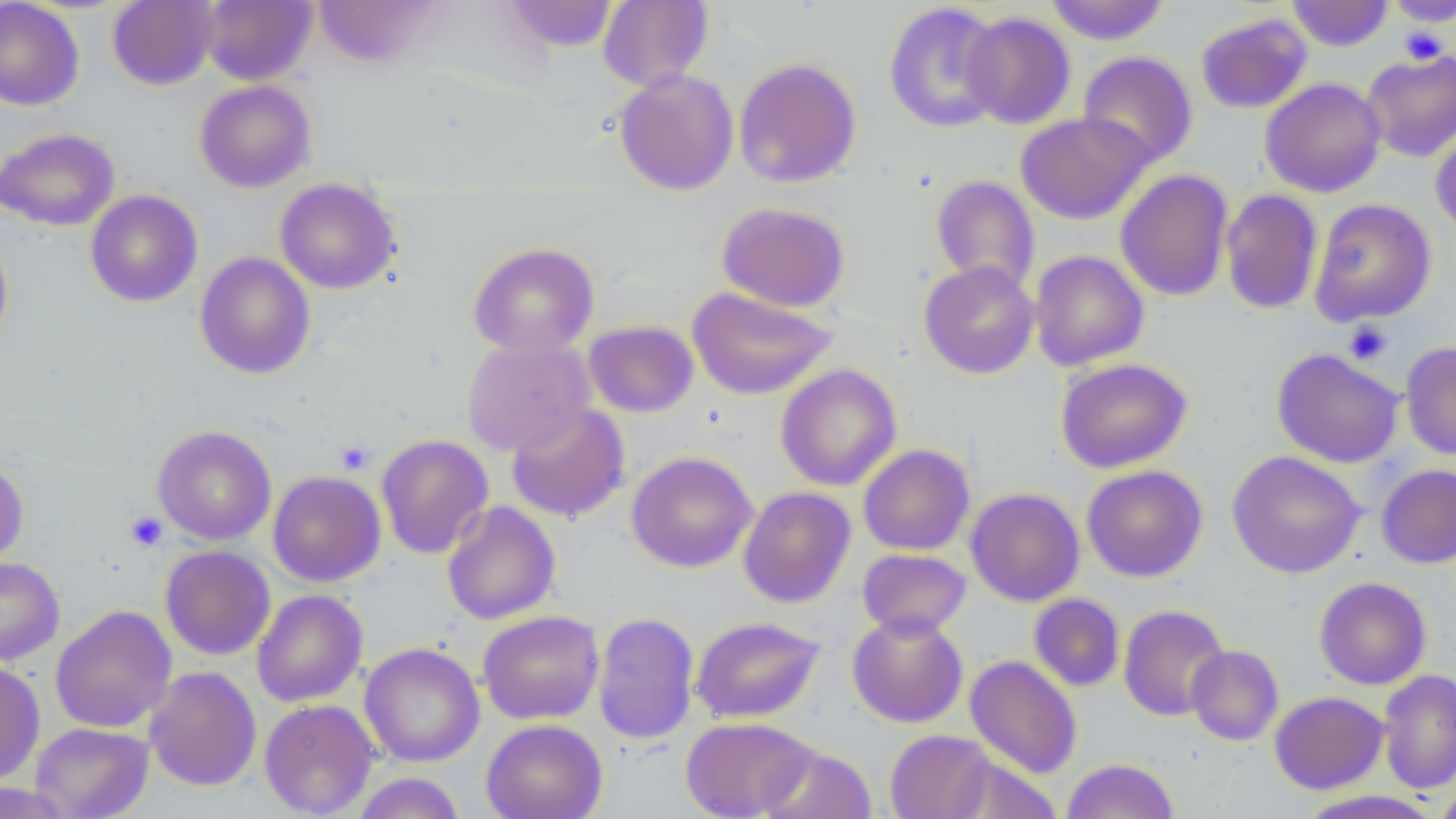

Approximate bounding boxes as (x1,y1)-(x2,y2) corner pairs in pixels. Uninfected red blood cell locations: (107,0)-(219,90), (200,0)-(316,86), (502,0)-(618,53), (598,0)-(713,92), (1046,0)-(1169,45), (1286,0)-(1394,52), (1384,0)-(1456,28), (0,1)-(85,111), (883,2)-(1005,133), (961,12)-(1076,129), (1195,12)-(1312,114), (1360,49)-(1456,162), (1077,51)-(1198,169), (734,58)-(861,188), (614,68)-(739,196), (1260,78)-(1387,197), (194,80)-(316,193), (1015,112)-(1153,224), (1430,120)-(1456,238), (0,127)-(120,231), (1115,169)-(1233,301), (931,175)-(1040,293), (274,178)-(402,294), (1220,189)-(1323,315), (84,190)-(202,308), (1309,198)-(1436,326), (717,201)-(850,312), (0,226)-(14,351), (467,241)-(599,357), (1029,250)-(1149,371), (195,252)-(316,379), (919,260)-(1039,379), (687,287)-(837,400), (584,320)-(699,417), (461,338)-(595,456), (1400,341)-(1456,460), (1272,348)-(1403,468), (1055,358)-(1192,473), (775,363)-(902,491), (505,402)-(631,523), (152,425)-(276,545), (376,433)-(494,559), (857,444)-(974,556), (1227,450)-(1364,578), (626,451)-(758,572), (0,458)-(29,565), (1376,463)-(1456,569), (1081,465)-(1207,582), (267,470)-(386,586), (738,486)-(856,608), (965,487)-(1085,607), (441,501)-(561,625), (160,545)-(275,660), (857,548)-(972,638), (0,556)-(65,666), (1314,576)-(1432,690), (252,589)-(368,707), (1028,593)-(1125,692), (1118,604)-(1231,721), (50,605)-(177,733), (478,610)-(605,724), (847,610)-(968,728), (593,612)-(700,746), (690,616)-(825,723), (360,642)-(484,767), (1186,645)-(1284,745), (965,655)-(1082,779), (0,659)-(45,785), (144,667)-(262,792), (1378,669)-(1456,794), (1269,691)-(1388,794), (259,699)-(379,817), (680,717)-(814,819), (481,719)-(607,819), (30,723)-(154,819), (884,729)-(996,819), (758,744)-(877,819), (946,756)-(1062,819), (1062,758)-(1179,819), (350,772)-(467,819), (0,782)-(73,818), (1433,784)-(1456,819), (1294,790)-(1444,819). Platelet locations: (1398,26)-(1450,65), (1343,321)-(1393,365), (334,439)-(376,476), (124,511)-(168,551). Slide-level diagnosis: negative for blood parasites. May-Grünwald-Giemsa-stained preparation. Thin blood film. Single field of view. Captured at 1000x magnification. Image is 1456×819 pixels. Optical microscopy.